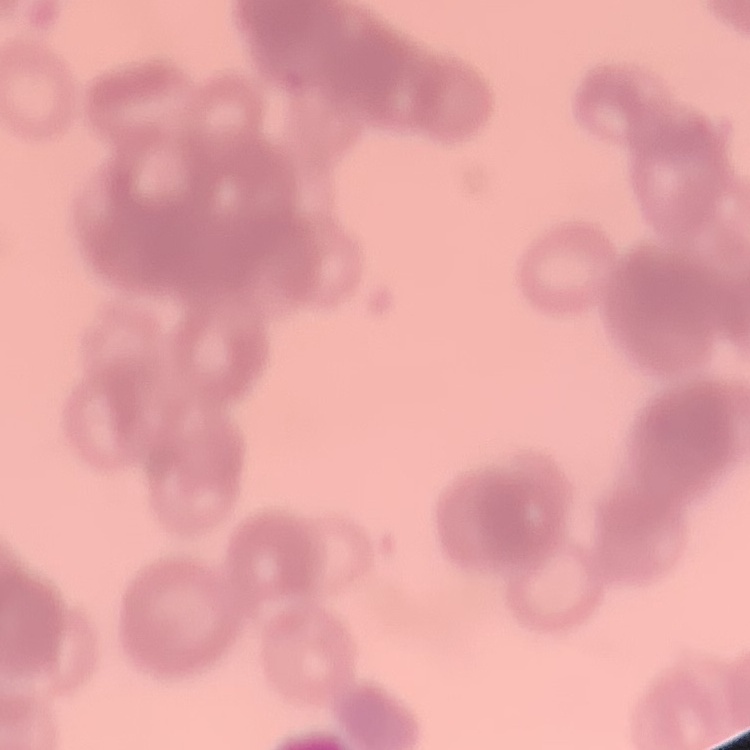

erythrocyte_morphology: rouleaux formation
preparation: thin blood smear
image_type: square crop of a larger photomicrograph
stain: Field's or Giemsa